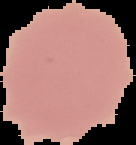

From a thin blood film. Image is 136×145 pixels. The area outside the segmented cell region is set to black. Result: negative for malaria parasites.